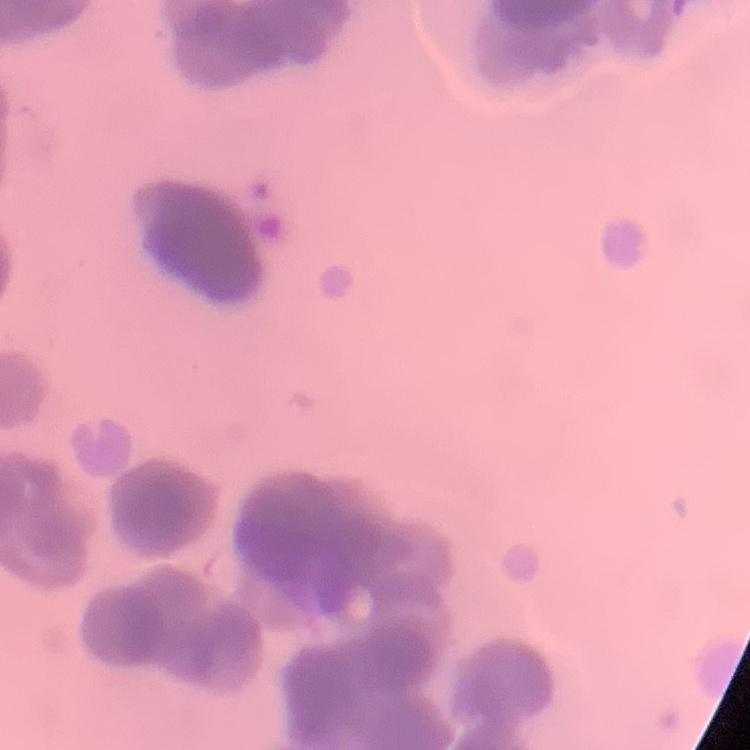 The red blood cells exhibit rouleaux formation. Stained with either Field's or Giemsa. Square crop of a larger photomicrograph. Thin peripheral smear.